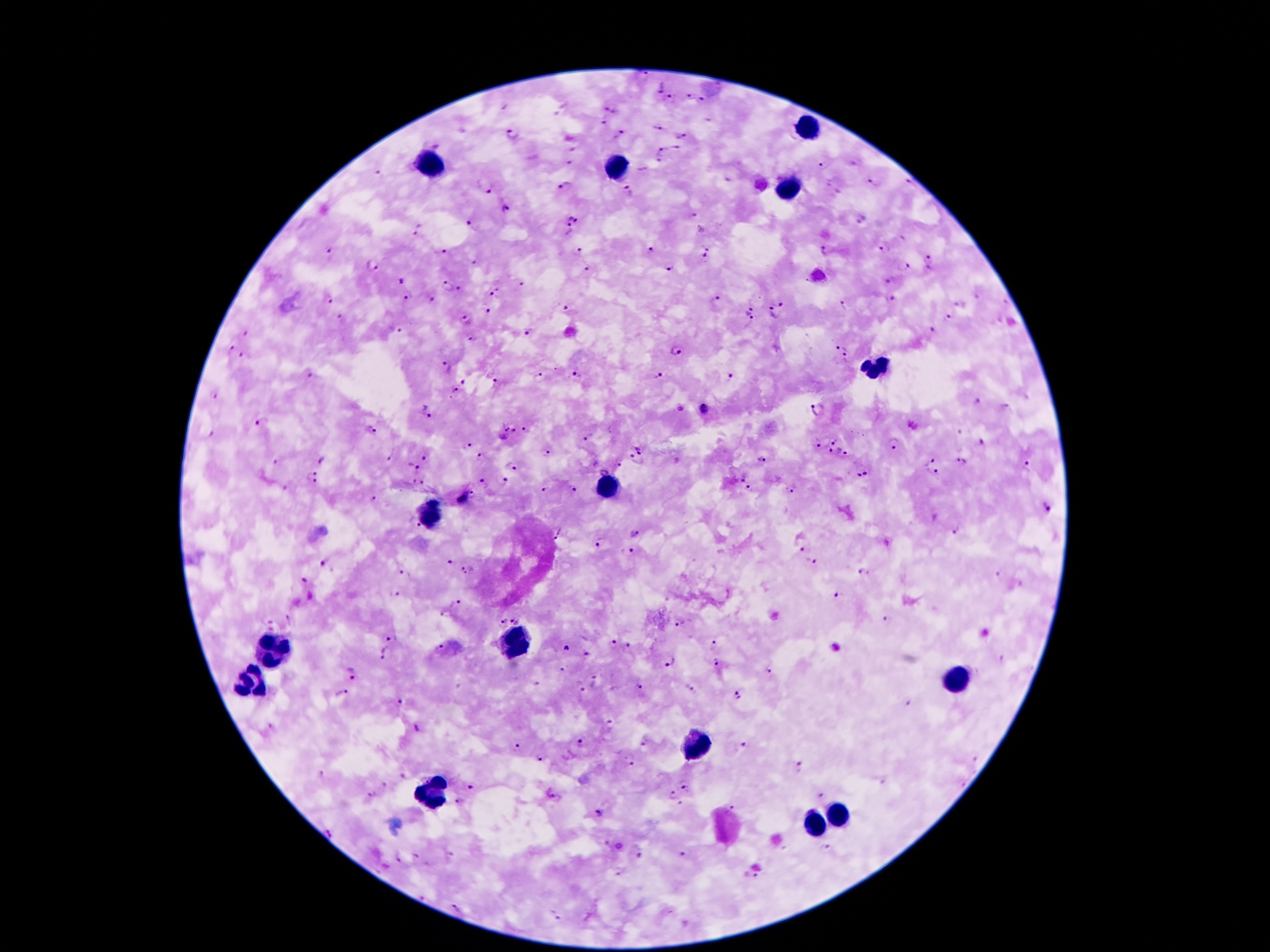

stain: Giemsa
patient_malaria_status: positive for Plasmodium falciparum
image_size: 1270×952 pixels
leukocyte_locations: 'approximate object centers, in pixels from the top-left corner: (x=806, y=127), (x=435, y=164), (x=615, y=170), (x=790, y=187), (x=874, y=367), (x=613, y=484), (x=431, y=515), (x=511, y=640), (x=273, y=650), (x=249, y=683), (x=960, y=683), (x=699, y=746), (x=431, y=795), (x=837, y=814), (x=814, y=824)'
preparation: thick blood smear
malaria_parasite_locations: 'approximate object centers, in pixels from the top-left corner: (x=660, y=85), (x=689, y=96), (x=671, y=97), (x=704, y=100), (x=610, y=108), (x=604, y=120), (x=658, y=128), (x=514, y=133), (x=683, y=135), (x=620, y=136), (x=677, y=149), (x=660, y=151), (x=571, y=163), (x=825, y=166), (x=378, y=174), (x=874, y=181), (x=908, y=183), (x=486, y=186), (x=563, y=187), (x=629, y=192), (x=505, y=210), (x=575, y=215), (x=694, y=218), (x=470, y=225), (x=419, y=229), (x=567, y=230), (x=706, y=245), (x=886, y=247), (x=654, y=248), (x=330, y=250), (x=824, y=251), (x=580, y=252), (x=441, y=253), (x=703, y=258), (x=929, y=260), (x=473, y=263), (x=902, y=264), (x=371, y=265), (x=671, y=267), (x=586, y=270), (x=400, y=280), (x=891, y=281), (x=521, y=284), (x=446, y=286), (x=461, y=291), (x=494, y=291), (x=406, y=296), (x=718, y=297), (x=328, y=298), (x=891, y=298), (x=430, y=301), (x=782, y=303), (x=846, y=304), (x=568, y=307), (x=485, y=308), (x=750, y=314), (x=772, y=314), (x=340, y=317), (x=949, y=318), (x=464, y=321), (x=395, y=329), (x=931, y=329), (x=527, y=332), (x=245, y=333), (x=472, y=339), (x=841, y=345), (x=230, y=348), (x=677, y=351), (x=245, y=355), (x=846, y=359), (x=446, y=366), (x=576, y=375), (x=657, y=375), (x=540, y=377), (x=731, y=377), (x=311, y=378), (x=464, y=382), (x=496, y=384), (x=454, y=390), (x=211, y=397), (x=977, y=402), (x=1006, y=407), (x=681, y=409), (x=703, y=409), (x=427, y=412), (x=817, y=412), (x=262, y=421), (x=374, y=431), (x=509, y=431), (x=527, y=431), (x=207, y=433), (x=958, y=433), (x=589, y=436), (x=835, y=440), (x=638, y=443), (x=823, y=443), (x=981, y=443), (x=466, y=444), (x=893, y=444), (x=835, y=452), (x=546, y=453), (x=849, y=453), (x=389, y=455), (x=424, y=457), (x=481, y=459), (x=928, y=459), (x=273, y=460), (x=761, y=460), (x=321, y=462), (x=638, y=462), (x=960, y=462), (x=618, y=465), (x=513, y=466), (x=1026, y=466), (x=412, y=467), (x=603, y=467), (x=932, y=474), (x=862, y=475), (x=311, y=477), (x=742, y=477), (x=501, y=481), (x=418, y=482), (x=481, y=482), (x=750, y=487), (x=285, y=489), (x=543, y=489), (x=573, y=490), (x=792, y=490), (x=473, y=496), (x=463, y=498), (x=374, y=500), (x=1045, y=506), (x=414, y=524), (x=957, y=527), (x=556, y=534), (x=635, y=535), (x=601, y=544), (x=629, y=550), (x=805, y=550), (x=450, y=563), (x=812, y=563), (x=324, y=565), (x=469, y=570), (x=864, y=572), (x=404, y=573), (x=303, y=581), (x=395, y=592), (x=839, y=595), (x=456, y=602), (x=292, y=619), (x=515, y=619), (x=501, y=620), (x=885, y=622), (x=679, y=623), (x=269, y=624), (x=392, y=639), (x=611, y=643), (x=715, y=645), (x=629, y=647), (x=439, y=649), (x=564, y=649), (x=384, y=652), (x=585, y=653), (x=667, y=660), (x=715, y=661), (x=564, y=669), (x=768, y=670), (x=346, y=674), (x=596, y=681), (x=579, y=686), (x=638, y=687), (x=689, y=688), (x=341, y=693), (x=740, y=693), (x=908, y=701), (x=400, y=703), (x=273, y=726), (x=417, y=728), (x=582, y=742), (x=645, y=744), (x=744, y=745), (x=517, y=746), (x=975, y=758), (x=539, y=760), (x=629, y=760), (x=801, y=770), (x=321, y=772), (x=403, y=777), (x=385, y=784), (x=472, y=786), (x=687, y=788), (x=370, y=794), (x=671, y=795), (x=820, y=795), (x=556, y=797), (x=459, y=802), (x=735, y=805), (x=600, y=813), (x=330, y=832), (x=826, y=850), (x=638, y=854), (x=451, y=855), (x=684, y=855), (x=399, y=860), (x=751, y=875), (x=459, y=906), (x=556, y=917)'
field_of_view: one from this slide
magnification: 100x
capture: smartphone through the microscope eyepiece